Comment on the morphology of the red blood cells.
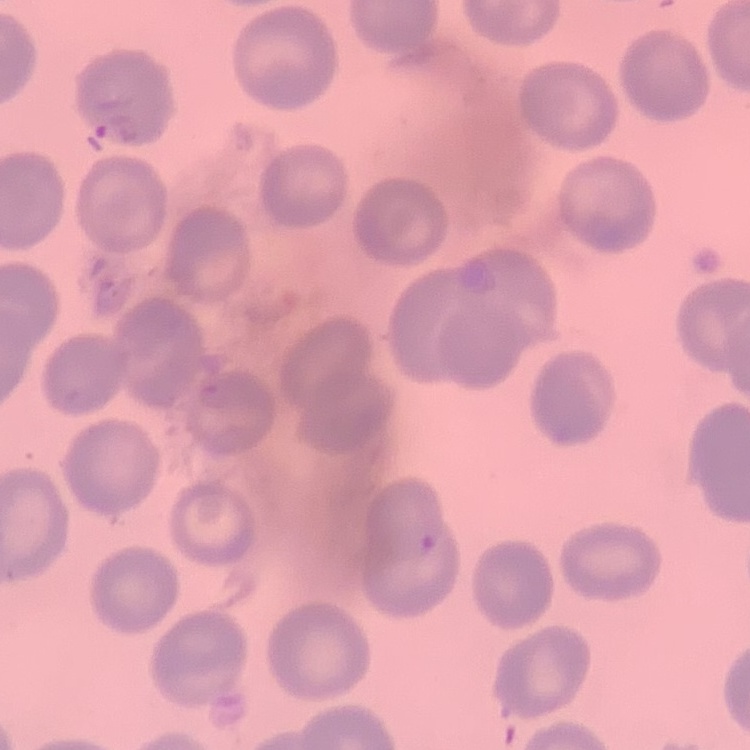

No rouleaux formation.

Square crop of a larger photomicrograph. Thin peripheral smear. Field's or Giemsa stain.